Mark where platelets are.
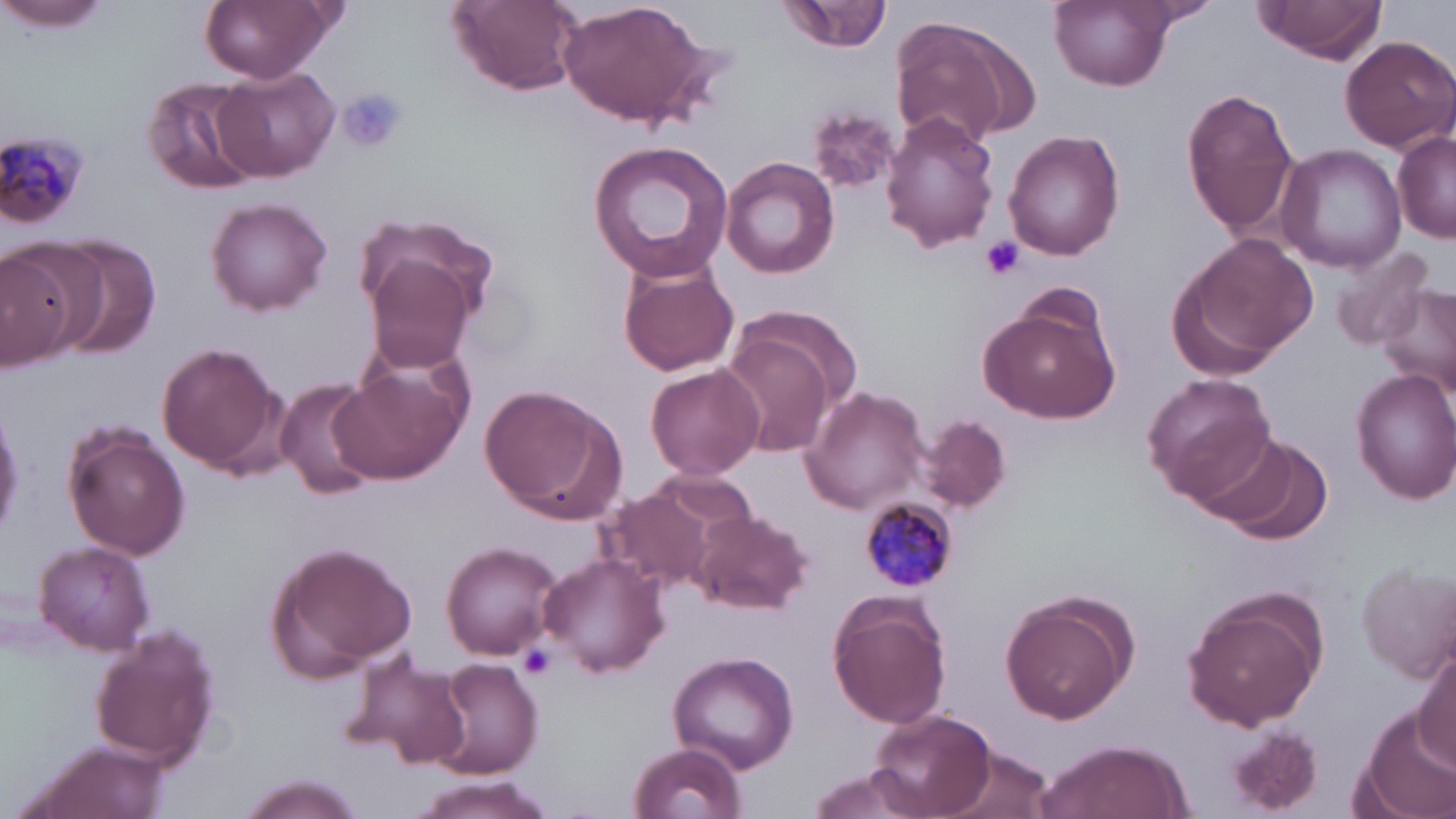

Approximate bounding boxes as [x1, y1, x2, y2] in pixels.
Platelets: [338, 88, 407, 151], [979, 236, 1026, 281], [517, 642, 557, 678].

{
  "slide_level_diagnosis": "Plasmodium malariae",
  "uninfected_red_blood_cell_locations": "approximate bounding boxes as [x1, y1, x2, y2] in pixels: [0, 0, 111, 32], [200, 0, 336, 83], [450, 0, 583, 94], [559, 0, 710, 129], [780, 0, 893, 55], [1049, 0, 1176, 90], [1252, 0, 1391, 62], [891, 13, 1035, 149], [1339, 35, 1454, 152], [214, 65, 340, 182], [140, 73, 262, 196], [1181, 87, 1300, 237], [810, 107, 898, 192], [880, 112, 999, 253], [1394, 130, 1456, 241], [1004, 131, 1126, 261], [589, 139, 733, 283], [1276, 142, 1405, 271], [720, 156, 838, 280], [204, 197, 331, 315], [355, 215, 498, 333], [1171, 234, 1315, 372], [53, 236, 162, 356], [0, 241, 90, 366], [1326, 244, 1434, 352], [359, 254, 475, 372], [618, 259, 742, 378], [1378, 282, 1456, 399], [734, 302, 867, 415], [977, 302, 1119, 423], [719, 332, 835, 459], [156, 343, 286, 476], [645, 362, 765, 481], [331, 367, 466, 482], [1352, 368, 1456, 504], [1143, 373, 1278, 505], [274, 378, 384, 502], [479, 382, 627, 525], [799, 386, 930, 515], [916, 416, 1011, 511], [60, 422, 190, 561], [1203, 434, 1331, 543], [598, 480, 741, 597], [689, 509, 813, 617], [33, 540, 156, 656], [264, 540, 417, 682], [441, 541, 564, 660], [539, 552, 669, 678], [1358, 560, 1456, 679], [1179, 586, 1330, 733], [826, 589, 952, 729], [999, 589, 1138, 725], [87, 625, 221, 770], [1413, 647, 1455, 767], [335, 651, 473, 773], [668, 651, 800, 771], [433, 657, 543, 778], [867, 707, 996, 816], [1354, 711, 1456, 819], [1225, 726, 1323, 814], [20, 738, 173, 819], [1033, 738, 1193, 819], [629, 740, 748, 819], [939, 747, 1056, 819], [805, 766, 928, 819], [237, 775, 368, 819], [411, 775, 555, 818]",
  "modality": "optical microscopy",
  "plasmodium_malariae_infected_red_blood_cell_locations": "approximate bounding boxes as [x1, y1, x2, y2] in pixels: [0, 126, 91, 230], [858, 497, 959, 594]",
  "preparation": "thin blood smear",
  "magnification": "1000x",
  "image_size": "1456×819 pixels",
  "field_of_view": "one of a larger specimen",
  "stain": "May-Grünwald-Giemsa"
}